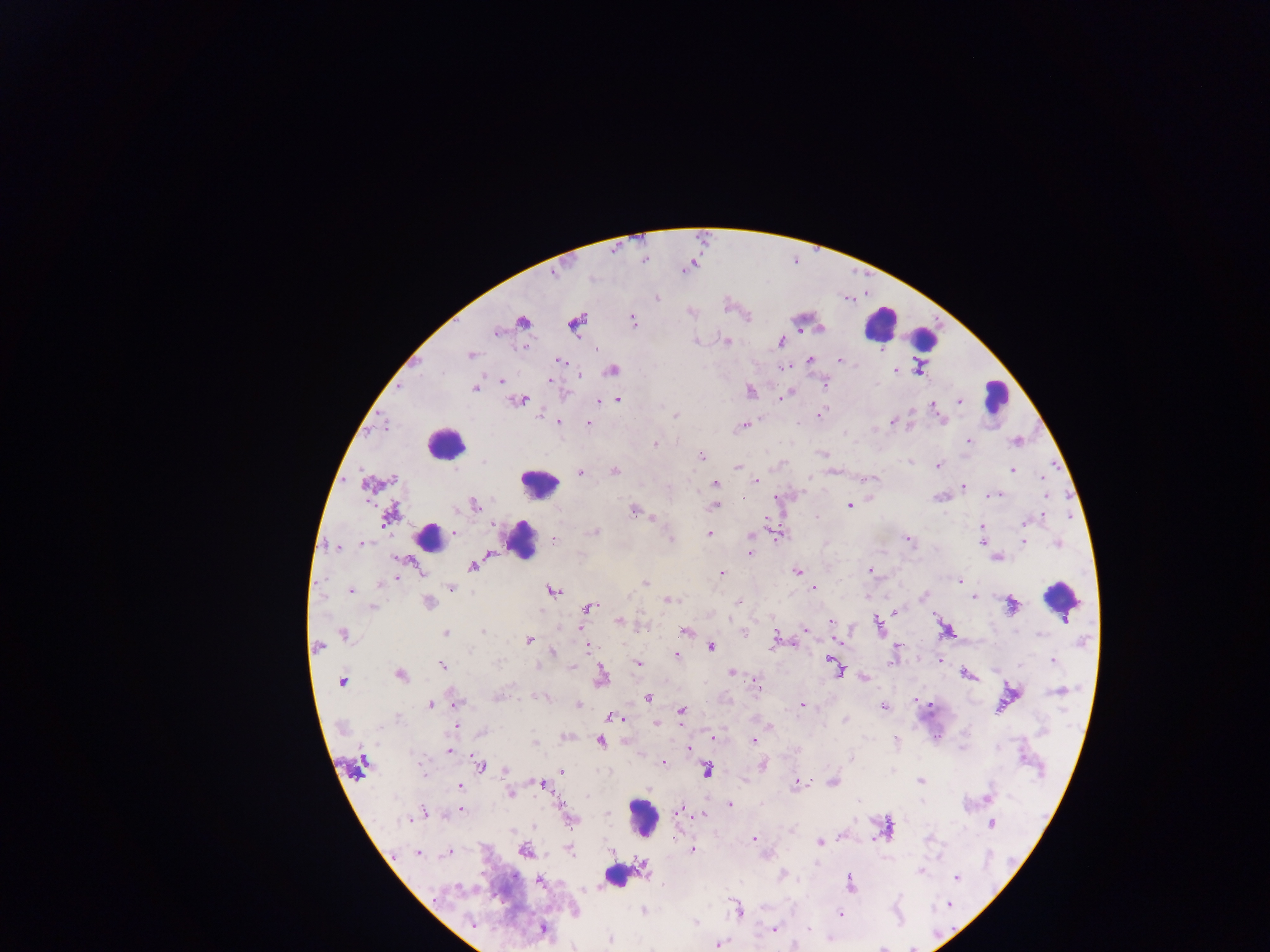

Approximate centers as {x, y} in pixels.
Summary:
  - Plasmodium parasite locations: {657, 298}, {521, 321}, {632, 321}, {575, 324}, {496, 333}, {695, 341}, {727, 341}, {780, 341}, {470, 354}, {809, 360}, {560, 361}, {840, 361}, {612, 371}, {895, 371}, {918, 371}, {551, 380}, {501, 381}, {824, 384}, {475, 388}, {750, 390}, {785, 396}, {617, 399}, {521, 400}, {960, 401}, {597, 402}, {933, 407}, {821, 413}, {676, 415}, {940, 420}, {558, 422}, {892, 422}, {588, 423}, {743, 426}, {968, 441}, {655, 444}, {823, 454}, {701, 455}, {938, 465}, {738, 467}, {1012, 469}, {614, 470}, {580, 473}, {1043, 476}, {874, 478}, {394, 479}, {756, 482}, {715, 484}, {366, 485}, {963, 487}, {994, 494}, {938, 497}, {1046, 497}, {869, 499}, {474, 505}, {850, 506}, {714, 507}, {633, 511}, {390, 514}, {816, 517}, {654, 518}, {1025, 522}, {982, 527}, {594, 532}, {455, 533}, {708, 533}, {776, 533}, {751, 535}, {671, 539}, {907, 540}, {554, 541}, {982, 541}, {1024, 542}, {1058, 543}, {362, 544}, {336, 547}, {750, 553}, {996, 558}, {473, 565}, {870, 571}, {797, 572}, {722, 573}, {396, 578}, {959, 581}, {645, 582}, {451, 588}, {814, 588}, {352, 591}, {553, 591}, {922, 596}, {973, 596}, {667, 600}, {739, 601}, {429, 603}, {1012, 606}, {373, 607}, {588, 607}, {894, 611}, {619, 621}, {831, 621}, {878, 622}, {805, 629}, {685, 631}, {482, 632}, {445, 633}, {344, 634}, {1040, 634}, {774, 636}, {529, 640}, {838, 641}, {588, 645}, {711, 646}, {318, 647}, {772, 647}, {552, 653}, {676, 655}, {939, 660}, {1053, 660}, {497, 661}, {637, 664}, {443, 666}, {537, 666}, {573, 667}, {837, 669}, {732, 673}, {400, 674}, {966, 674}, {602, 676}, {864, 679}, {342, 682}, {759, 688}, {1059, 691}, {496, 697}, {648, 698}, {917, 700}, {457, 702}, {577, 704}, {430, 705}, {803, 705}, {885, 707}, {681, 711}, {612, 716}, {398, 719}, {846, 720}, {656, 723}, {456, 726}, {714, 738}, {754, 740}, {896, 740}, {601, 742}, {534, 743}, {689, 748}, {448, 751}, {851, 759}, {663, 762}, {361, 765}, {480, 765}, {763, 765}, {506, 770}, {562, 770}, {707, 770}, {833, 781}, {921, 781}, {798, 782}, {542, 785}, {460, 787}, {510, 794}, {989, 796}, {730, 804}, {461, 810}, {678, 812}, {423, 814}, {607, 814}, {704, 815}, {408, 819}, {991, 824}, {886, 829}, {513, 831}, {754, 839}, {674, 840}, {819, 842}, {692, 849}, {524, 851}, {611, 851}, {570, 852}, {447, 854}, {419, 855}, {920, 872}, {783, 873}, {957, 878}, {540, 880}, {851, 882}, {949, 905}, {643, 911}, {738, 911}, {841, 914}, {695, 922}, {473, 924}, {542, 929}, {774, 929}, {809, 929}, {610, 939}, {718, 945}, {881, 948}
  - Leukocyte locations: {880, 324}, {924, 338}, {996, 395}, {446, 443}, {539, 483}, {429, 537}, {521, 539}, {1060, 599}, {643, 818}, {623, 874}
  - Image size: 1270×952 pixels
  - Capture: mobile-phone photograph through a microscope
  - Preparation: thick blood smear
  - Country: Ghana
  - Field of view: single